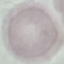

Summary:
  - Malaria status: uninfected
  - Capture: smartphone through the microscope eyepiece
  - Stain: Giemsa
  - Preparation: thin blood smear
  - Image type: cell patch, automatically extracted from a larger field of view and resized to 64 × 64 pixels